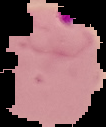
Image is 106×127 pixels. Cell region segmented out of the field of view; the surrounding area is masked to black. Result: Plasmodium parasites identified. From a thin blood film.